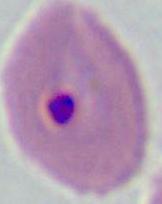

400x or 1000x magnification. Photomicrograph. A Plasmodium parasite is shown.